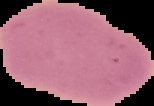

Summary:
  - Preparation: thin blood film
  - Image size: 154×106 pixels
  - Result: negative for malaria parasites
  - Image type: cell region segmented out of the field of view; surrounding area masked to black